State which cell type is depicted.
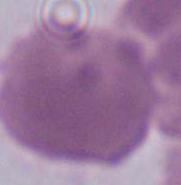
An erythrocyte.

Summary:
  - Magnification: 1000x
  - Modality: photomicrograph